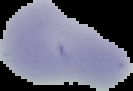

preparation = thin blood smear
image type = segmented cell region with the area outside set to black
result = no malaria parasites detected
image size = 133×91 pixels